Locate platelets.
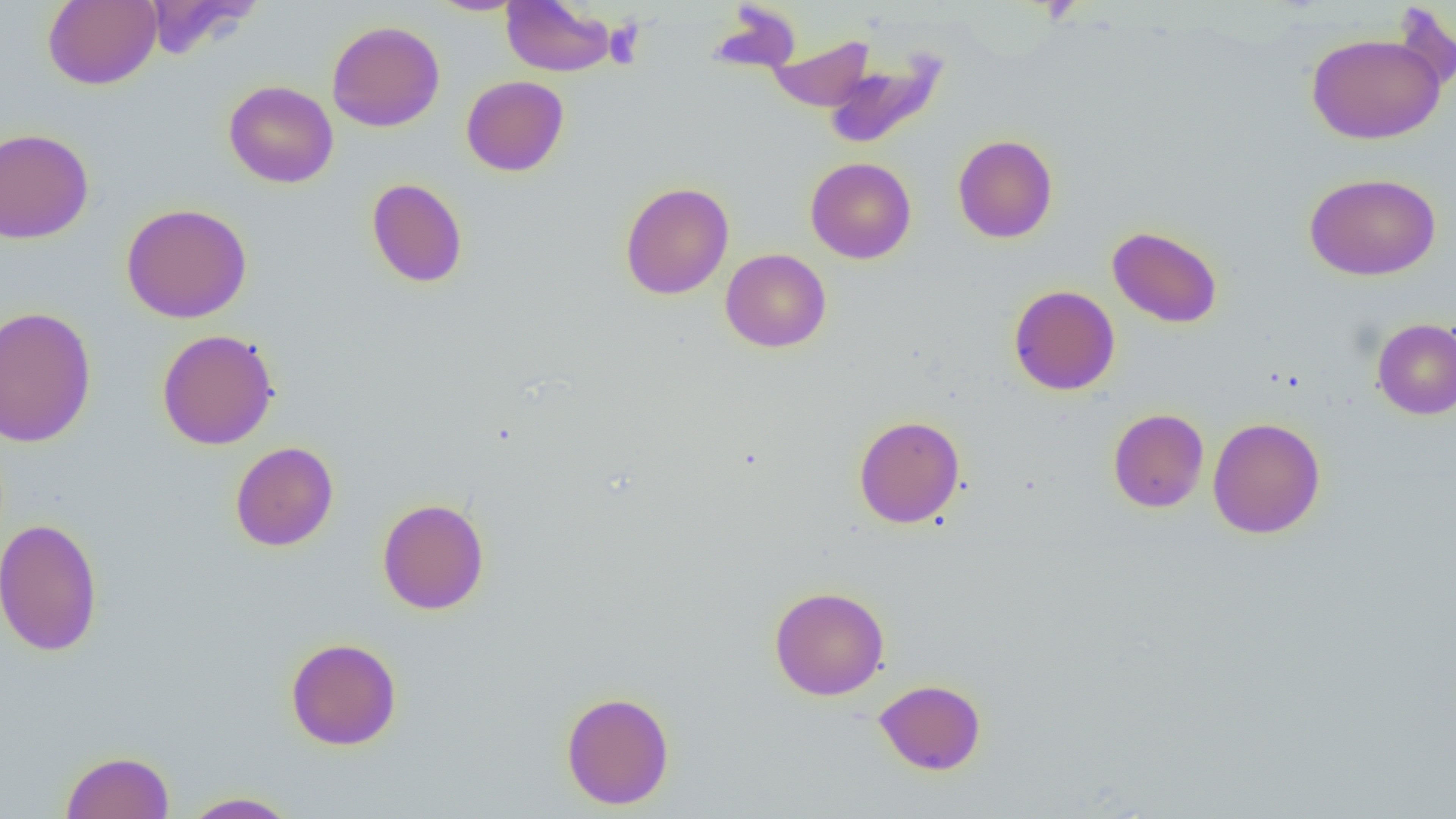
Approximate bounding boxes as named x1/y1/x2/y2 corners in pixels.
Platelets: (x1=604, y1=19, x2=646, y2=68).

Uninfected red blood cell locations: (x1=42, y1=0, x2=161, y2=90), (x1=140, y1=0, x2=262, y2=58), (x1=429, y1=1, x2=527, y2=16), (x1=501, y1=1, x2=616, y2=77), (x1=327, y1=20, x2=445, y2=132), (x1=1306, y1=32, x2=1446, y2=144), (x1=767, y1=34, x2=874, y2=112), (x1=822, y1=49, x2=949, y2=150), (x1=461, y1=75, x2=569, y2=176), (x1=224, y1=80, x2=338, y2=188), (x1=0, y1=127, x2=94, y2=244), (x1=953, y1=134, x2=1058, y2=243), (x1=805, y1=157, x2=916, y2=263), (x1=1304, y1=172, x2=1441, y2=280), (x1=367, y1=178, x2=468, y2=288), (x1=620, y1=181, x2=734, y2=300), (x1=121, y1=203, x2=252, y2=323), (x1=1107, y1=225, x2=1222, y2=328), (x1=720, y1=248, x2=831, y2=353), (x1=1009, y1=285, x2=1120, y2=395), (x1=0, y1=306, x2=97, y2=447), (x1=1371, y1=318, x2=1456, y2=420), (x1=156, y1=329, x2=279, y2=450), (x1=1108, y1=408, x2=1209, y2=512), (x1=853, y1=415, x2=965, y2=529), (x1=1208, y1=417, x2=1326, y2=539), (x1=230, y1=441, x2=339, y2=551), (x1=377, y1=498, x2=490, y2=615), (x1=1, y1=517, x2=103, y2=657), (x1=769, y1=586, x2=890, y2=700), (x1=285, y1=637, x2=401, y2=751), (x1=874, y1=679, x2=986, y2=775), (x1=561, y1=691, x2=675, y2=810), (x1=60, y1=750, x2=175, y2=819), (x1=181, y1=791, x2=300, y2=818). Slide-level diagnosis: negative for blood parasites. One field of a larger specimen. Image is 1456×819 pixels. Captured at 1000x magnification. Thin blood smear. Optical microscopy.